Identify the blood parasite species.
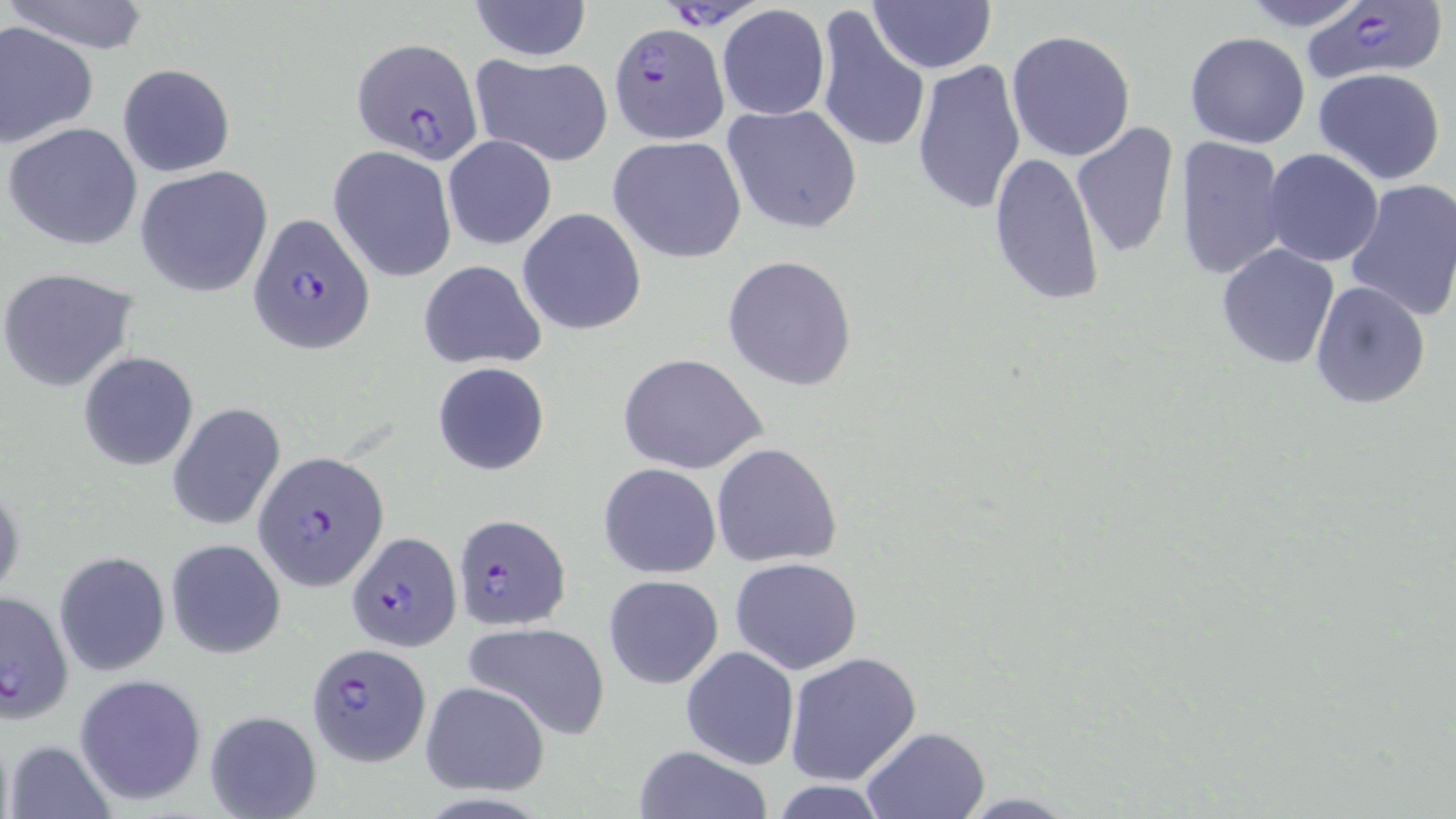
Plasmodium falciparum.

Summary:
  - Coordinate format: approximate bounding boxes as (x1,y1)-(x2,y2) corner pairs in pixels
  - Uninfected red blood cell locations: (2,0)-(153,54), (468,0)-(592,61), (867,0)-(998,73), (1233,0)-(1378,31), (716,5)-(830,119), (812,11)-(926,154), (0,21)-(98,147), (1005,29)-(1136,162), (1184,32)-(1311,149), (467,53)-(614,167), (911,59)-(1026,217), (117,63)-(235,177), (1313,68)-(1447,185), (723,102)-(863,234), (1070,120)-(1178,260), (4,121)-(143,250), (442,135)-(557,250), (608,136)-(747,265), (1174,137)-(1288,280), (328,147)-(457,282), (1262,149)-(1383,266), (988,151)-(1104,306), (136,165)-(274,298), (1344,179)-(1456,322), (518,208)-(647,335), (1215,243)-(1340,370), (721,256)-(858,391), (417,261)-(547,368), (0,267)-(140,393), (1308,279)-(1432,410), (79,351)-(198,472), (617,352)-(768,474), (432,361)-(551,477), (168,402)-(285,532), (711,443)-(842,568), (598,462)-(722,579), (0,477)-(23,604), (166,539)-(285,658), (54,552)-(170,677), (730,557)-(864,675), (602,574)-(725,690), (462,620)-(611,740), (681,646)-(799,769), (784,651)-(922,786), (74,675)-(206,807), (419,680)-(551,796), (204,708)-(323,819), (861,727)-(989,818), (4,737)-(114,819), (631,745)-(773,819), (766,781)-(894,818)
  - Plasmodium falciparum-infected red blood cell locations: (665,0)-(760,33), (1299,0)-(1447,84), (608,22)-(728,143), (350,37)-(484,163), (249,213)-(374,354), (252,454)-(385,592), (449,512)-(570,631), (348,530)-(461,652), (1,590)-(73,720), (305,642)-(431,765)
  - Modality: light microscopy
  - Magnification: 1000x
  - Stain: May-Grünwald-Giemsa
  - Preparation: thin blood smear
  - Field of view: one of a larger specimen
  - Image size: 1456×819 pixels